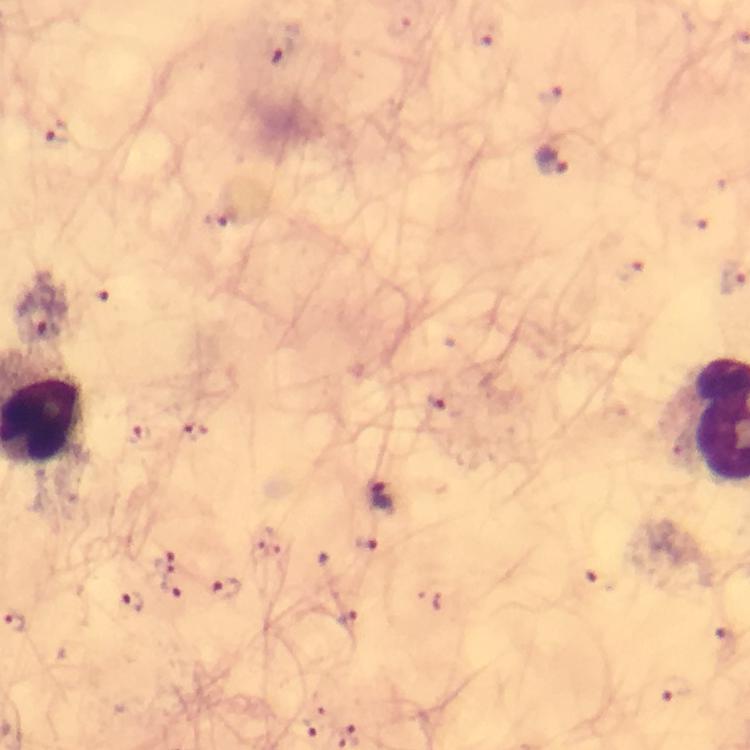

stain = Giemsa
preparation = thick blood film
image size = 750×750 pixels
capture = smartphone photograph through a microscope
magnification = 100x
immersion oil = used
cropped from = a single field of view
malaria parasite locations = approximate object centers, in pixels from the top-left corner: (x=486, y=34), (x=278, y=51), (x=550, y=97), (x=56, y=133), (x=553, y=161), (x=222, y=222), (x=633, y=272), (x=101, y=298), (x=435, y=402), (x=194, y=433), (x=137, y=435), (x=383, y=496), (x=363, y=545), (x=164, y=563), (x=600, y=581), (x=170, y=590), (x=224, y=590), (x=132, y=604), (x=347, y=618), (x=726, y=639), (x=676, y=690)
context = from a diagnostic examination for malaria